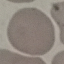
Summary:
  - Malaria status: uninfected
  - Image type: automatically extracted cell patch, resized to 64 × 64 pixels
  - Stain: Giemsa
  - Preparation: thin smear
  - Capture: smartphone through the microscope eyepiece